Locate every uninfected red blood cell.
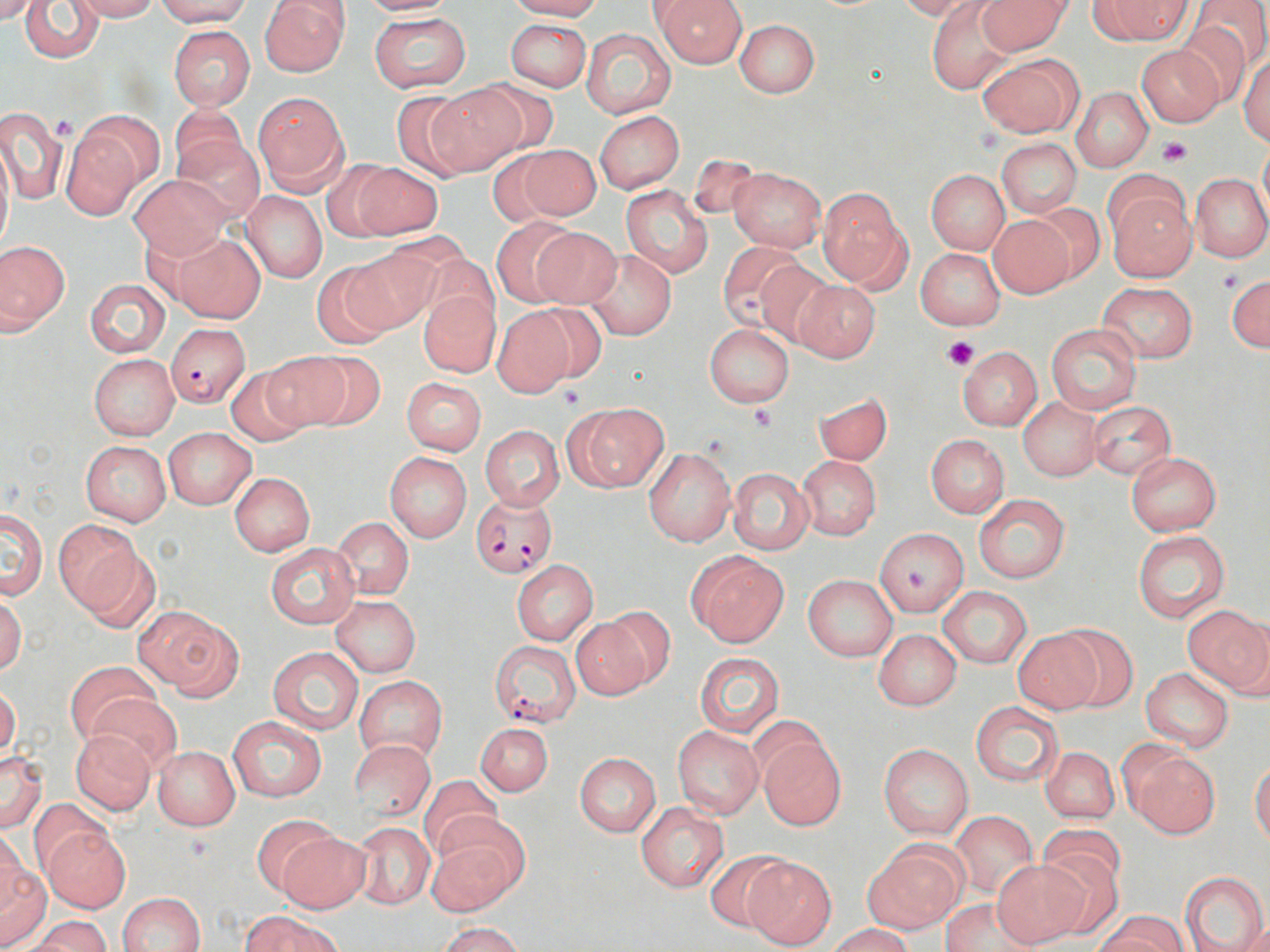
Approximate bounding boxes as (x1, y1, x2, y2) in pixels.
Uninfected red blood cells: (0, 0, 41, 26), (20, 0, 106, 63), (71, 0, 161, 21), (154, 0, 252, 26), (258, 0, 350, 76), (355, 0, 459, 16), (502, 0, 604, 20), (655, 0, 747, 67), (977, 0, 1072, 56), (1095, 0, 1194, 44), (1193, 0, 1270, 72), (895, 1, 976, 20), (926, 2, 1015, 95), (368, 12, 471, 92), (1172, 17, 1256, 106), (505, 19, 592, 91), (734, 19, 820, 98), (167, 24, 255, 111), (580, 27, 677, 120), (1136, 45, 1223, 127), (1238, 53, 1270, 146), (978, 54, 1082, 137), (467, 79, 561, 160), (428, 83, 527, 173), (1072, 87, 1153, 171), (387, 90, 481, 180), (253, 92, 349, 192), (170, 106, 251, 189), (0, 108, 67, 205), (72, 109, 167, 196), (594, 111, 683, 193), (174, 132, 263, 220), (62, 133, 142, 220), (996, 138, 1082, 218), (1259, 138, 1270, 220), (0, 139, 13, 258), (506, 144, 601, 224), (322, 162, 398, 241), (353, 163, 443, 239), (726, 165, 827, 253), (926, 169, 1009, 254), (127, 173, 233, 260), (1190, 173, 1270, 262), (622, 185, 712, 280), (1105, 185, 1197, 281), (818, 186, 908, 288), (241, 190, 327, 283), (1026, 203, 1105, 285), (988, 214, 1075, 297), (490, 217, 582, 306), (528, 226, 621, 310), (170, 233, 267, 324), (1, 241, 69, 332), (718, 241, 812, 334), (342, 248, 440, 334), (916, 248, 1006, 330), (416, 249, 501, 334), (584, 249, 676, 340), (755, 260, 837, 349), (312, 264, 397, 349), (1225, 273, 1269, 352), (85, 279, 170, 357), (793, 280, 880, 363), (1098, 282, 1198, 363), (418, 288, 500, 377), (523, 303, 609, 387), (492, 307, 575, 396), (704, 324, 794, 407), (1045, 324, 1141, 414), (957, 345, 1044, 431), (259, 351, 353, 432), (297, 351, 386, 430), (88, 355, 179, 440), (225, 365, 314, 447), (402, 376, 486, 455), (814, 391, 892, 466), (1018, 399, 1100, 481), (1088, 402, 1177, 480), (566, 403, 667, 492), (479, 425, 564, 510), (164, 428, 255, 510), (925, 435, 1009, 516), (81, 440, 171, 526), (642, 446, 736, 547), (384, 452, 471, 542), (1126, 452, 1221, 535), (797, 455, 880, 540), (728, 468, 813, 554), (229, 472, 315, 555), (974, 495, 1070, 583), (1, 507, 48, 599), (332, 517, 414, 599), (55, 520, 144, 617), (875, 527, 970, 617), (1131, 530, 1230, 622), (73, 544, 164, 633), (267, 544, 359, 628), (687, 551, 788, 646), (511, 561, 598, 644), (802, 575, 897, 661), (937, 586, 1032, 669), (0, 591, 26, 677), (331, 596, 421, 676), (1184, 605, 1269, 696), (599, 607, 678, 690), (137, 608, 241, 697), (569, 614, 656, 700), (1055, 623, 1139, 710), (1014, 628, 1103, 714), (873, 629, 961, 710), (268, 647, 364, 735), (694, 652, 785, 737), (66, 660, 159, 746), (1140, 668, 1235, 751), (355, 676, 446, 764), (0, 685, 20, 763), (89, 692, 180, 773), (971, 701, 1065, 786), (227, 715, 327, 802), (475, 722, 553, 796), (672, 726, 763, 817), (71, 729, 156, 815), (756, 733, 847, 830), (349, 739, 436, 822), (879, 745, 973, 839), (151, 746, 240, 831), (1122, 746, 1218, 838), (1041, 747, 1119, 824), (0, 750, 46, 833), (574, 752, 661, 835), (1250, 758, 1270, 846), (417, 774, 502, 861), (30, 799, 110, 875), (635, 802, 730, 893), (949, 812, 1038, 901), (250, 815, 338, 900), (350, 820, 435, 910), (427, 820, 526, 915), (1037, 822, 1127, 898), (42, 824, 131, 912), (0, 828, 25, 914), (274, 831, 371, 914), (863, 844, 965, 933), (1034, 849, 1125, 939), (703, 850, 792, 933), (742, 856, 837, 950), (992, 861, 1089, 947), (0, 864, 52, 950), (1181, 871, 1268, 952), (118, 892, 205, 952), (939, 897, 1039, 951), (243, 911, 341, 952), (1096, 912, 1187, 952), (21, 915, 111, 952), (435, 922, 523, 952), (829, 924, 913, 952).

slide-level diagnosis = Plasmodium falciparum
stain = May-Grünwald-Giemsa
image size = 1270×952 pixels
preparation = thin blood film
field of view = one of a larger specimen
Plasmodium falciparum-infected red blood cell locations = approximate bounding boxes as (x1, y1, x2, y2) in pixels: (166, 322, 251, 404), (472, 493, 558, 578), (490, 641, 580, 727)
magnification = 1000x
modality = light microscopy
platelet locations = approximate bounding boxes as (x1, y1, x2, y2) in pixels: (52, 115, 80, 143), (1156, 137, 1191, 167), (1216, 270, 1244, 295), (943, 336, 980, 369), (559, 385, 586, 409), (748, 405, 777, 430)